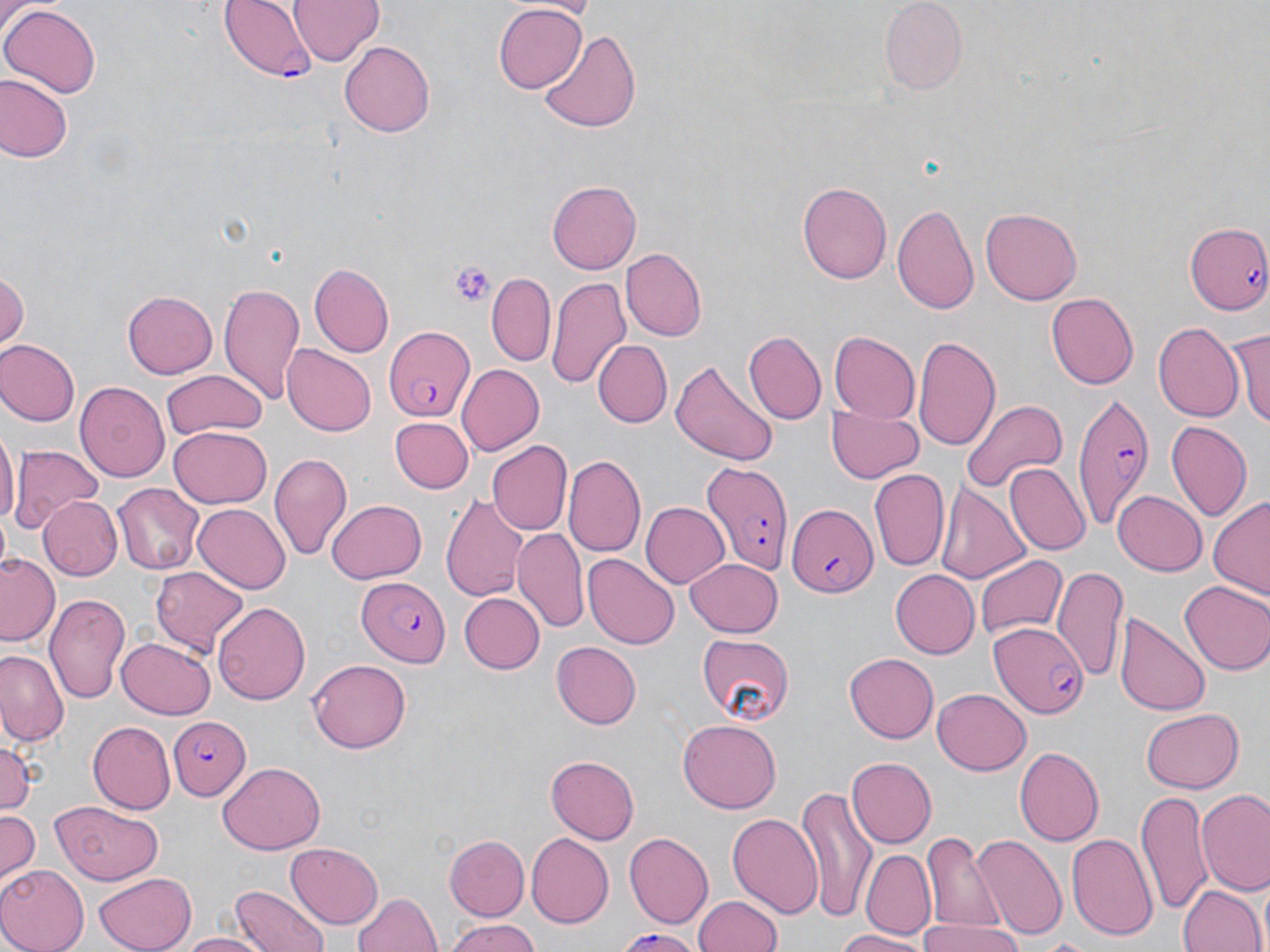

slide-level diagnosis = Plasmodium falciparum
magnification = 1000x
image size = 1270×952 pixels
uninfected red blood cell locations = approximate bounding boxes as (x1, y1, x2, y2) in pixels: (289, 0, 384, 64), (881, 0, 966, 93), (0, 3, 102, 100), (492, 5, 587, 93), (537, 29, 645, 135), (339, 41, 434, 136), (0, 75, 73, 163), (799, 180, 892, 286), (548, 181, 641, 272), (892, 204, 978, 317), (981, 207, 1083, 305), (621, 247, 706, 342), (309, 263, 394, 357), (0, 268, 27, 351), (487, 274, 555, 364), (546, 275, 631, 389), (218, 282, 307, 407), (122, 291, 217, 378), (1046, 292, 1137, 389), (1231, 322, 1270, 432), (1153, 323, 1243, 423), (828, 331, 921, 423), (743, 332, 827, 425), (912, 333, 1002, 455), (1, 340, 80, 426), (594, 340, 672, 427), (282, 342, 376, 436), (668, 360, 777, 466), (456, 364, 545, 455), (161, 370, 266, 442), (75, 382, 169, 483), (962, 398, 1068, 492), (828, 408, 923, 483), (391, 417, 474, 493), (1167, 421, 1252, 522), (167, 425, 271, 510), (0, 433, 17, 533), (488, 440, 572, 536), (12, 445, 103, 533), (268, 453, 353, 561), (564, 455, 645, 557), (1004, 463, 1089, 553), (870, 468, 951, 573), (113, 482, 208, 575), (935, 482, 1030, 588), (1112, 489, 1206, 576), (440, 490, 531, 606), (1207, 495, 1270, 603), (39, 497, 121, 579), (328, 499, 425, 583), (641, 501, 731, 589), (194, 504, 289, 595), (512, 527, 590, 635), (583, 553, 678, 649), (1, 554, 60, 647), (975, 554, 1066, 640), (686, 557, 782, 636), (1052, 563, 1128, 688), (152, 567, 247, 655), (889, 570, 980, 658), (1178, 577, 1270, 676), (45, 591, 131, 706), (457, 592, 543, 675), (213, 599, 309, 704), (1114, 611, 1209, 717), (696, 634, 795, 721), (116, 637, 215, 719), (551, 640, 641, 728), (0, 651, 68, 743), (845, 654, 939, 743), (309, 658, 409, 754), (932, 687, 1031, 778), (1140, 708, 1246, 792), (676, 720, 782, 813), (89, 721, 176, 813), (0, 736, 37, 816), (1015, 747, 1103, 846), (546, 755, 639, 844), (847, 756, 937, 849), (218, 763, 325, 853), (797, 787, 873, 921), (1198, 788, 1270, 893), (1138, 791, 1212, 915), (50, 802, 166, 886), (0, 809, 40, 886), (728, 809, 824, 919), (924, 831, 1004, 934), (1067, 831, 1158, 941), (524, 832, 613, 928), (626, 832, 715, 928), (971, 833, 1067, 942), (442, 834, 528, 921), (285, 843, 385, 927), (861, 847, 934, 938), (0, 867, 88, 952), (94, 869, 195, 952), (1178, 880, 1264, 952), (229, 885, 331, 952), (352, 890, 442, 952), (694, 894, 783, 951), (444, 918, 541, 952), (918, 919, 1022, 952), (833, 929, 934, 951), (612, 930, 703, 949), (177, 932, 274, 952), (1036, 937, 1089, 947)
field of view = one of a larger specimen
platelet locations = approximate bounding boxes as (x1, y1, x2, y2) in pixels: (450, 260, 497, 305)
preparation = thin blood smear
modality = light microscopy
stain = May-Grünwald-Giemsa
Plasmodium falciparum-infected red blood cell locations = approximate bounding boxes as (x1, y1, x2, y2) in pixels: (218, 0, 314, 82), (1184, 221, 1270, 311), (381, 326, 476, 421), (1070, 394, 1152, 530), (699, 459, 792, 576), (785, 501, 879, 599), (357, 575, 450, 666), (989, 625, 1089, 719), (171, 717, 251, 800)